Locate and identify every blood parasite.
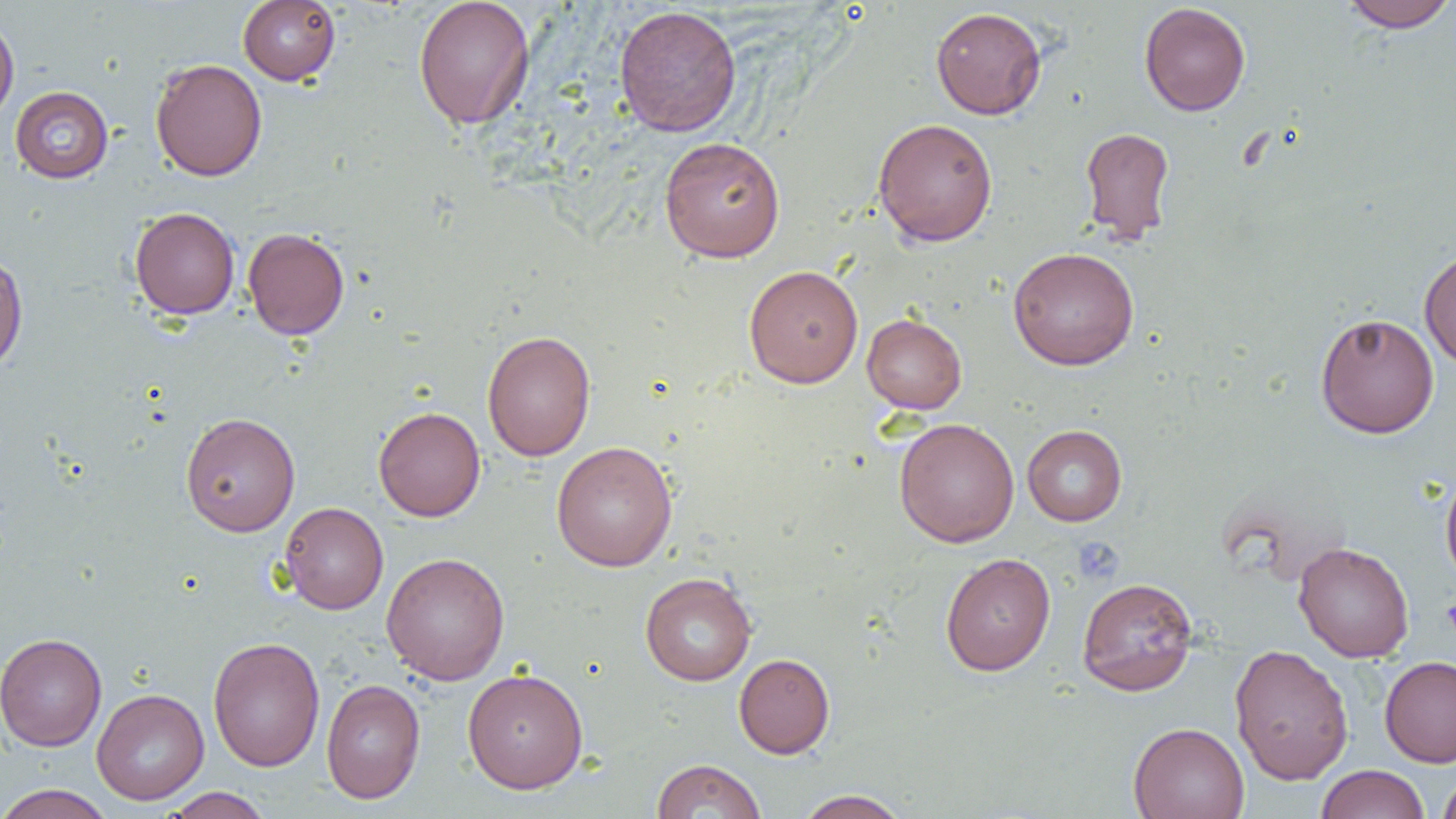

No blood parasites observed.

slide-level diagnosis = negative for blood parasites
modality = light microscopy
uninfected red blood cell locations = approximate bounding boxes as [x1, y1, x2, y2] in pixels: [238, 0, 341, 85], [413, 0, 535, 130], [1338, 0, 1456, 33], [1139, 2, 1251, 116], [614, 5, 742, 137], [930, 7, 1047, 119], [0, 14, 19, 124], [150, 58, 267, 181], [10, 86, 113, 183], [873, 117, 998, 247], [1080, 127, 1175, 245], [658, 136, 786, 263], [129, 207, 240, 320], [242, 227, 350, 340], [1008, 246, 1139, 370], [1419, 248, 1456, 369], [0, 250, 28, 373], [743, 264, 863, 388], [862, 313, 967, 414], [1315, 313, 1440, 438], [482, 330, 596, 461], [373, 406, 486, 521], [180, 412, 301, 537], [894, 417, 1019, 547], [1022, 425, 1127, 526], [551, 441, 677, 571], [1440, 466, 1456, 590], [280, 502, 389, 614], [1293, 541, 1414, 662], [381, 551, 510, 685], [939, 552, 1056, 676], [640, 572, 757, 686], [1077, 576, 1198, 696], [1, 632, 107, 751], [208, 636, 325, 773], [1229, 643, 1354, 786], [734, 653, 835, 758], [1379, 655, 1456, 768], [462, 667, 588, 794], [321, 678, 426, 804], [91, 688, 209, 805], [1128, 722, 1250, 819], [651, 758, 766, 818], [1315, 764, 1430, 819], [1437, 771, 1456, 819], [0, 784, 116, 819], [163, 787, 273, 818], [795, 789, 911, 818]
field of view = single
platelet locations = approximate bounding boxes as [x1, y1, x2, y2] in pixels: [1073, 536, 1125, 584], [1442, 597, 1456, 636]
preparation = thin blood smear
magnification = 1000x
image size = 1456×819 pixels